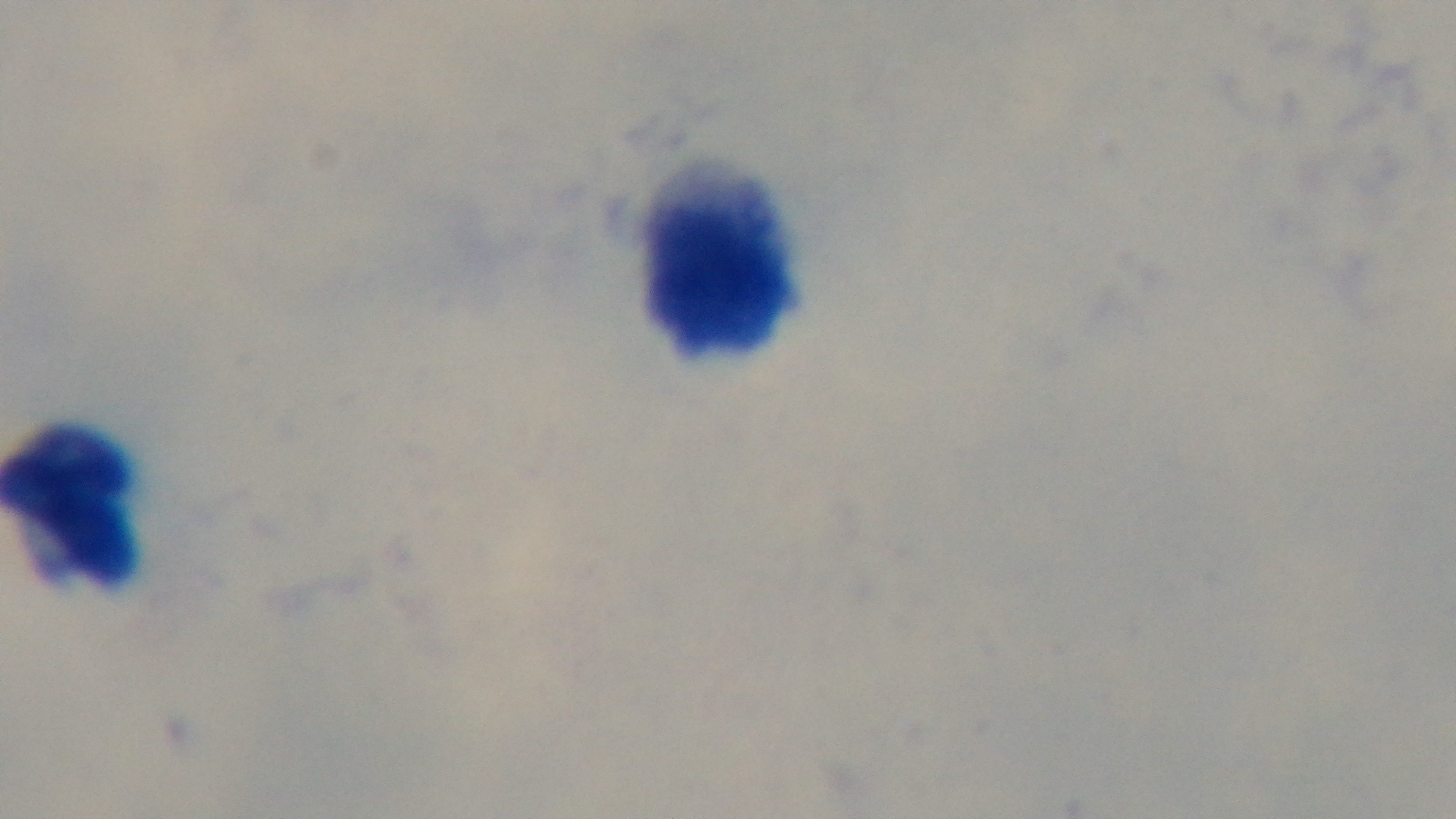

Mounted 4K digital camera. Malaria status: uninfected. One field from the slide. Light microscopy. Preparation: thick smear. 100x oil-immersion objective. Giemsa stain.